Classify this cell by malaria status.
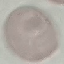

It is uninfected.

Acquired by smartphone through the microscope eyepiece. Giemsa-stained preparation. Cell patch, automatically extracted from a larger field of view and resized to 64 × 64 pixels. Thin blood film.